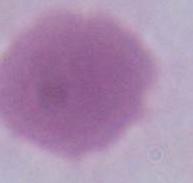

{
  "identification": "red blood cell",
  "magnification": "1000x",
  "modality": "photomicrograph"
}